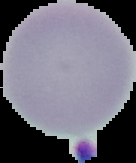

Summary:
  - Image size: 136×163 pixels
  - Malaria status: uninfected
  - Image type: segmented cell region with the area outside set to black
  - Preparation: thin blood film